Report the malaria status of this cell.
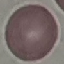

Uninfected.

Summary:
  - Capture: smartphone through the microscope eyepiece
  - Preparation: thin smear
  - Stain: Giemsa
  - Image type: cell patch, automatically extracted from a larger field of view and resized to 64 × 64 pixels